State which parasite is depicted.
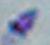

Toxoplasma gondii.

magnification = 1000x
modality = micrograph